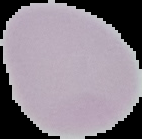

Result: negative for malaria parasites. Image is 142×139 pixels. From a thin blood smear. Segmented cell region on a black background.